Report the malaria status of this cell.
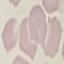
It is uninfected.

Summary:
  - Preparation: thin blood film
  - Stain: Giemsa
  - Image type: cell patch, automatically extracted from a larger field of view and resized to 64 × 64 pixels
  - Capture: smartphone through the microscope eyepiece